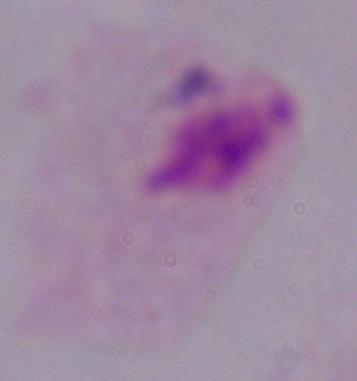 A trichomonad is shown. Photomicrograph. 1000x magnification.